Assess this cell for malaria.
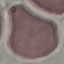
It is uninfected.

Summary:
  - Preparation: thin blood smear
  - Capture: smartphone through the microscope eyepiece
  - Image type: cell patch, automatically extracted from a larger field of view and resized to 64 × 64 pixels
  - Stain: Giemsa